Give the location of every parasitized red blood cell.
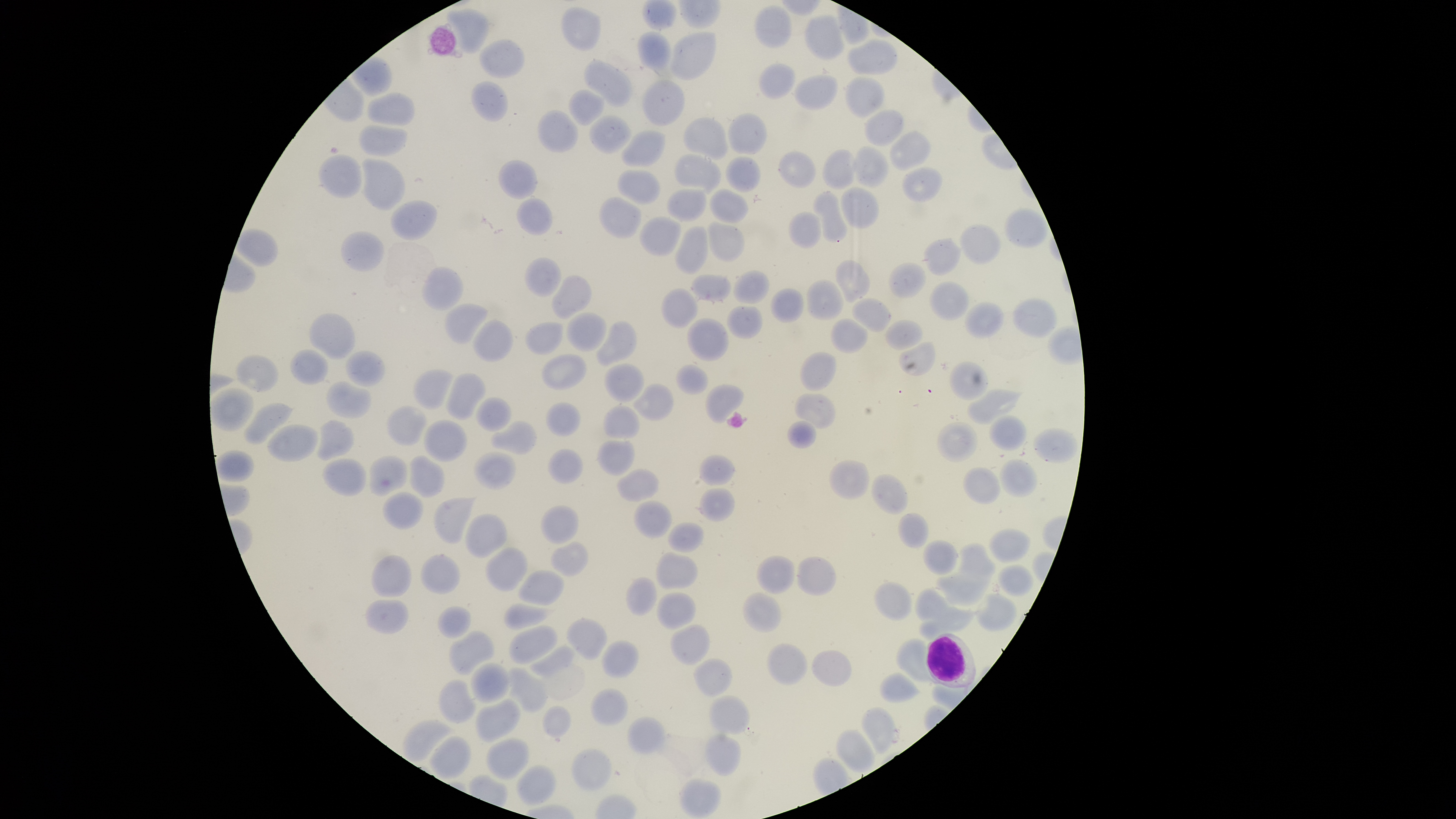

No parasitized red blood cells identified.

Approximate bounding boxes as [left, top, right, bottom] in pixels.
Summary:
  - White blood cells: [925, 632, 977, 689]
  - Uninfected red blood cells: [642, 0, 678, 31], [754, 4, 792, 49], [560, 6, 601, 52], [445, 7, 490, 54], [804, 15, 847, 60], [636, 31, 672, 71], [670, 31, 717, 81], [478, 38, 525, 78], [847, 39, 897, 75], [584, 58, 633, 108], [757, 64, 795, 100], [793, 75, 839, 111], [844, 76, 885, 118], [642, 78, 685, 126], [471, 81, 508, 122], [568, 89, 605, 126], [367, 91, 415, 126], [863, 109, 905, 146], [536, 110, 580, 153], [726, 112, 767, 155], [588, 115, 632, 153], [682, 117, 728, 160], [358, 124, 408, 157], [621, 129, 667, 168], [889, 131, 930, 170], [852, 146, 889, 188], [777, 149, 817, 189], [822, 149, 857, 190], [318, 153, 362, 199], [674, 153, 721, 195], [724, 156, 761, 191], [360, 157, 406, 212], [498, 160, 539, 199], [901, 167, 944, 203], [617, 169, 660, 204], [841, 187, 879, 229], [709, 188, 749, 224], [666, 189, 707, 223], [811, 190, 848, 244], [598, 196, 642, 239], [517, 198, 553, 236], [390, 200, 438, 241], [1004, 207, 1048, 249], [788, 210, 822, 249], [638, 215, 682, 257], [706, 220, 746, 262], [959, 224, 1001, 264], [674, 225, 709, 275], [235, 228, 279, 268], [341, 231, 384, 272], [923, 237, 963, 276], [524, 256, 562, 296], [836, 259, 871, 302], [888, 263, 926, 298], [421, 265, 464, 311], [732, 270, 770, 304], [691, 272, 732, 303], [550, 275, 591, 320], [806, 279, 844, 320], [928, 280, 969, 321], [660, 287, 698, 329], [770, 288, 804, 323], [851, 297, 891, 334], [1011, 297, 1058, 338], [443, 301, 488, 345], [964, 301, 1005, 339], [726, 305, 763, 339], [308, 312, 356, 360], [565, 312, 607, 352], [471, 318, 514, 363], [687, 318, 729, 361], [830, 318, 869, 353], [596, 320, 638, 367], [885, 320, 923, 350], [524, 321, 564, 355], [898, 341, 936, 377], [290, 349, 328, 385], [345, 351, 385, 387], [799, 351, 837, 391], [541, 353, 586, 390], [235, 354, 279, 393], [949, 360, 988, 401], [603, 362, 644, 402], [676, 364, 708, 395], [412, 368, 454, 410], [446, 372, 486, 421], [326, 380, 373, 419], [632, 383, 674, 421], [705, 384, 744, 424], [211, 387, 254, 432], [966, 388, 1024, 426], [793, 393, 836, 429], [475, 397, 512, 433], [243, 402, 294, 445], [545, 402, 580, 436], [386, 405, 427, 446], [603, 405, 640, 439], [988, 415, 1028, 451], [315, 419, 354, 461], [423, 419, 467, 462], [489, 420, 537, 455], [786, 420, 817, 449], [936, 421, 978, 462], [267, 423, 319, 463], [1032, 429, 1078, 464], [599, 442, 634, 473], [214, 449, 255, 483], [547, 449, 584, 485], [473, 451, 516, 491], [409, 454, 445, 497], [698, 454, 736, 486], [368, 455, 408, 497], [322, 457, 366, 496], [828, 460, 869, 501], [999, 460, 1038, 498], [615, 467, 660, 502], [962, 467, 1001, 505], [870, 473, 908, 515], [697, 488, 736, 522], [381, 491, 423, 529], [433, 496, 477, 544], [633, 499, 672, 538], [540, 504, 579, 544], [897, 512, 930, 549], [465, 514, 508, 558], [667, 522, 704, 553], [988, 528, 1032, 562], [922, 539, 958, 575], [550, 540, 589, 576], [956, 542, 997, 584], [485, 547, 528, 592], [655, 551, 698, 590], [419, 553, 460, 595], [371, 555, 413, 598], [755, 555, 796, 594], [797, 556, 837, 596], [997, 564, 1035, 597], [517, 570, 564, 606], [936, 573, 989, 606], [626, 576, 658, 616], [873, 581, 912, 621], [914, 586, 967, 623], [743, 591, 782, 633], [656, 592, 696, 629], [974, 594, 1018, 632], [364, 599, 409, 634], [503, 603, 556, 631], [437, 605, 472, 639], [919, 606, 981, 640], [566, 618, 607, 660], [670, 624, 710, 666], [508, 625, 557, 665], [448, 630, 496, 676], [895, 638, 933, 684], [602, 640, 639, 679], [766, 642, 809, 687], [529, 645, 575, 679], [810, 650, 852, 687], [692, 658, 733, 698], [470, 661, 510, 705], [508, 666, 548, 712], [879, 672, 922, 703], [439, 678, 476, 724], [590, 688, 628, 725], [709, 694, 750, 736], [475, 698, 521, 743], [542, 705, 571, 738], [860, 705, 896, 753], [627, 716, 666, 755], [401, 719, 455, 763], [834, 729, 876, 773], [704, 733, 742, 776], [428, 736, 471, 779], [485, 737, 530, 780], [570, 749, 612, 792], [516, 764, 557, 806], [679, 778, 722, 817]
  - Field of view: single
  - Preparation: thin smear of blood
  - Image size: 1456×819 pixels
  - Capture: smartphone photograph through the microscope eyepiece
  - Visible region: circular
  - Stain: Giemsa